Assess this cell for malaria.
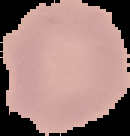
It is uninfected.

Image is 130×136 pixels. Segmented cell region on a black background. From a thin blood smear.